State which parasite is depicted.
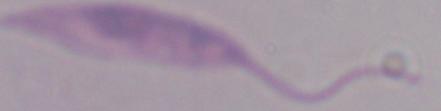
Leishmania.

Captured at 1000x magnification. Micrograph.